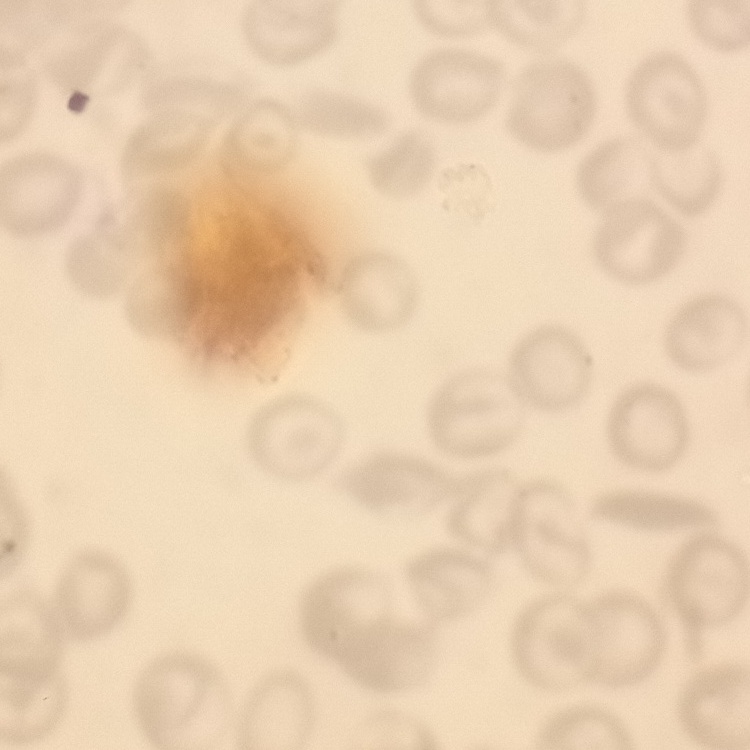
erythrocyte morphology = no rouleaux formation
stain = Field's or Giemsa
image type = one tile cut from a larger photomicrograph
preparation = thin blood film